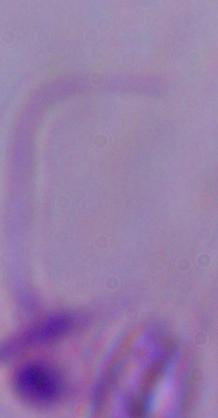
magnification = 1000x
modality = micrograph
identification = Leishmania